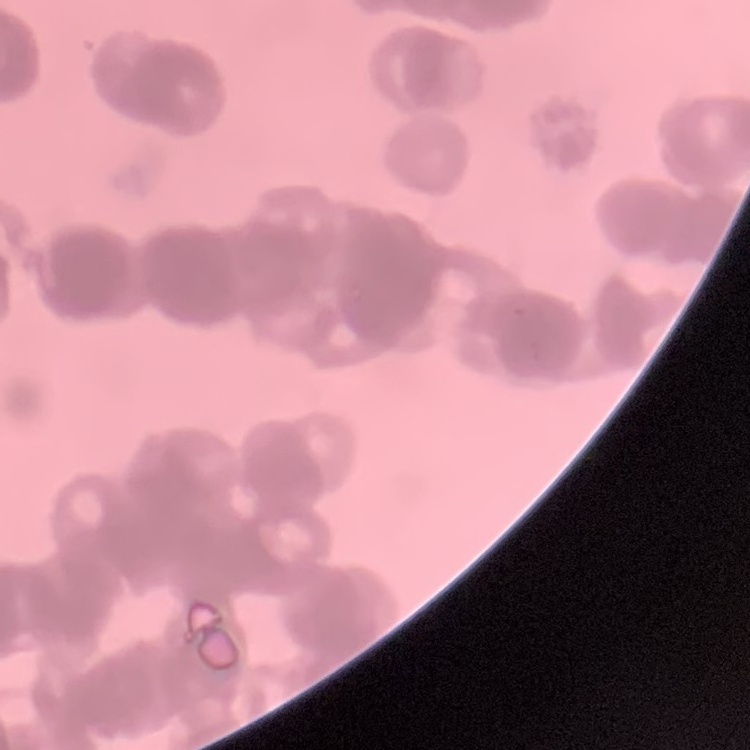
The erythrocytes exhibit rouleaux formation. Thin blood smear. Stained with either Field's or Giemsa. Square crop of a larger photomicrograph.